Name the cell type shown.
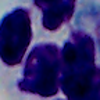

This is a leukocyte.

Summary:
  - Magnification: 1000x
  - Modality: micrograph